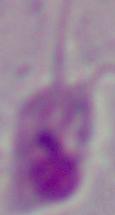
{
  "identification": "Leishmania",
  "magnification": "1000x",
  "modality": "micrograph"
}